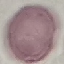
Malaria status: uninfected. Acquired by smartphone through the microscope eyepiece. Giemsa-stained preparation. Thin smear of blood. Cell patch, automatically extracted from a larger field of view and resized to 64 × 64 pixels.